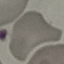

Result: negative for malaria parasites. Giemsa stain. Photographed with a smartphone camera at the microscope eyepiece. Thin smear of blood. Cell patch, automatically extracted from a larger field of view and resized to 64 × 64 pixels.